Find the red blood cells and label each as P. falciparum-infected, uninfected, or of indeterminate infection status.
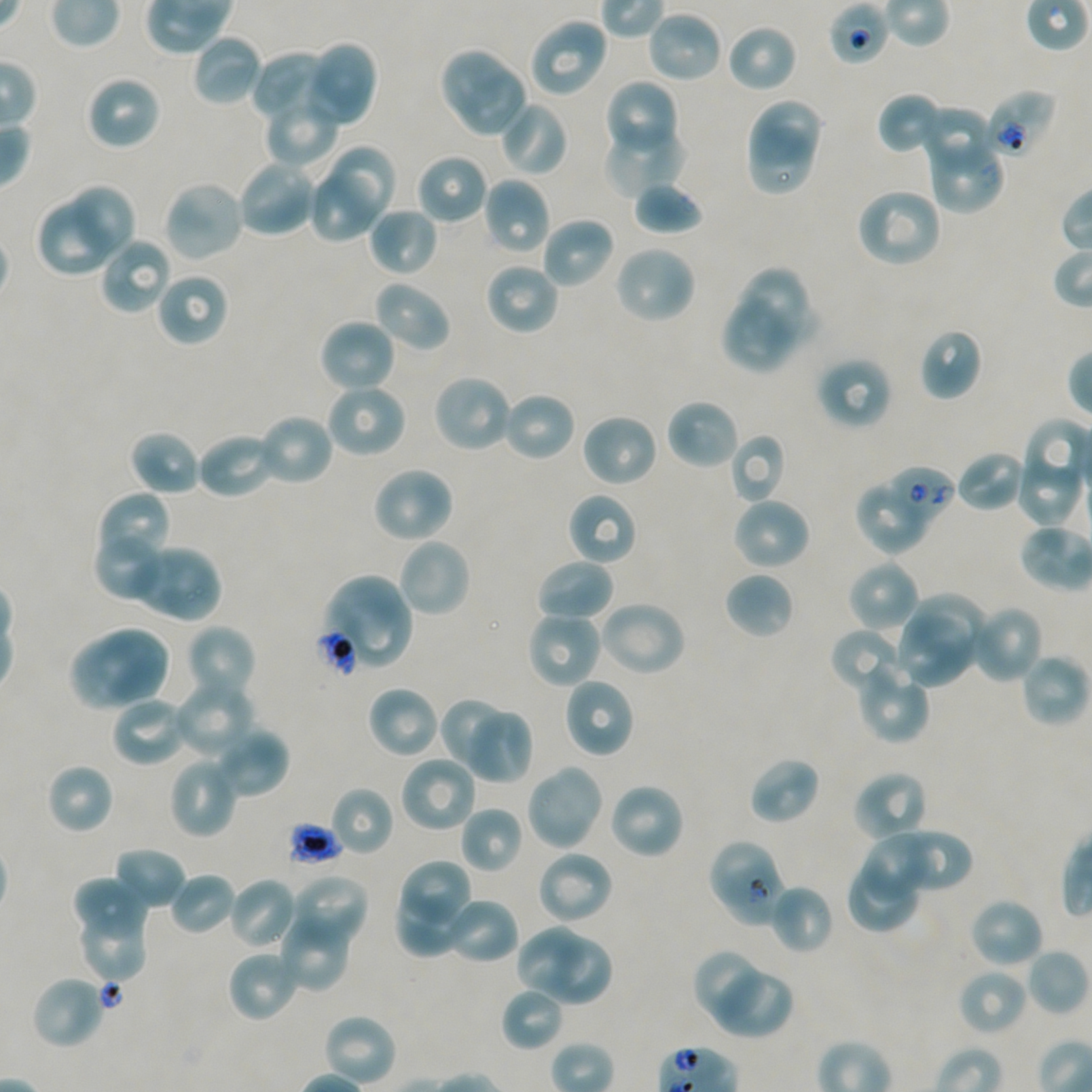

Approximate bounding boxes as {x1, y1, x2, y2} in pixels. Not every red blood cell is marked.
Red blood cells of indeterminate infection status: {829, 1, 891, 65}, {985, 89, 1057, 160}, {925, 134, 1004, 213}, {888, 465, 956, 522}, {315, 627, 359, 678}, {707, 837, 776, 911}, {726, 864, 785, 926}.
Uninfected red blood cells: {646, 10, 724, 84}, {528, 16, 608, 99}, {726, 23, 798, 94}, {192, 33, 263, 108}, {304, 41, 378, 128}, {438, 46, 509, 115}, {251, 50, 331, 123}, {458, 67, 526, 138}, {86, 75, 162, 151}, {603, 79, 680, 159}, {877, 92, 947, 155}, {263, 96, 339, 168}, {744, 96, 820, 165}, {498, 100, 569, 177}, {918, 103, 997, 173}, {602, 123, 686, 199}, {748, 130, 812, 193}, {329, 146, 396, 220}, {416, 153, 489, 225}, {236, 158, 319, 238}, {312, 175, 376, 241}, {481, 176, 551, 255}, {633, 179, 704, 236}, {162, 180, 246, 263}, {71, 185, 133, 256}, {855, 186, 943, 269}, {36, 200, 111, 278}, {368, 206, 439, 277}, {540, 216, 616, 290}, {98, 236, 173, 316}, {612, 244, 697, 325}, {484, 262, 560, 337}, {739, 266, 807, 338}, {155, 272, 230, 347}, {372, 280, 451, 353}, {721, 295, 794, 374}, {318, 317, 397, 394}, {919, 327, 983, 401}, {816, 356, 893, 431}, {432, 373, 515, 454}, {325, 382, 407, 459}, {501, 390, 577, 462}, {665, 397, 740, 471}, {255, 412, 335, 487}, {580, 412, 659, 488}, {128, 429, 202, 497}, {196, 431, 278, 500}, {729, 433, 788, 504}, {956, 450, 1027, 513}, {1015, 462, 1082, 526}, {370, 465, 455, 545}, {857, 486, 926, 553}, {98, 490, 166, 560}, {566, 491, 639, 566}, {731, 496, 811, 571}, {96, 535, 158, 597}, {397, 536, 472, 619}, {126, 543, 221, 623}, {535, 558, 615, 624}, {848, 559, 920, 633}, {723, 571, 795, 640}, {323, 573, 414, 672}, {913, 593, 985, 667}, {598, 600, 687, 678}, {969, 604, 1045, 684}, {526, 610, 602, 689}, {895, 612, 975, 688}, {184, 623, 257, 704}, {830, 627, 909, 695}, {95, 629, 168, 700}, {68, 638, 145, 712}, {1019, 653, 1089, 729}, {855, 659, 930, 744}, {562, 676, 636, 759}, {172, 677, 257, 759}, {367, 685, 441, 759}, {109, 694, 190, 768}, {438, 697, 509, 774}, {471, 711, 534, 784}, {213, 724, 290, 799}, {399, 754, 479, 834}, {748, 755, 820, 825}, {168, 757, 239, 839}, {45, 762, 115, 835}, {524, 763, 604, 852}, {852, 770, 929, 845}, {608, 782, 686, 861}, {329, 786, 395, 857}, {460, 805, 524, 874}, {903, 827, 972, 887}, {865, 833, 930, 903}, {112, 846, 187, 911}, {535, 849, 615, 926}, {404, 861, 468, 922}, {845, 865, 916, 934}, {169, 872, 237, 936}, {293, 874, 370, 946}, {228, 876, 300, 951}, {72, 877, 146, 938}, {768, 883, 835, 955}, {399, 886, 471, 956}, {441, 896, 520, 965}, {968, 896, 1044, 970}, {75, 898, 149, 983}, {276, 911, 352, 994}, {513, 924, 583, 993}, {549, 936, 612, 1005}, {227, 948, 302, 1023}, {1026, 948, 1089, 1017}, {694, 951, 759, 1019}, {714, 968, 793, 1037}, {957, 968, 1028, 1036}, {30, 974, 108, 1050}, {500, 986, 564, 1052}, {323, 1013, 397, 1087}.
No infected red blood cells observed.

Donor blood group A+/O+. Static in-vitro culture of P. falciparum strain NF54. Oil immersion, 100x objective (numerical aperture 1.45). Image is 1092×1092 pixels. Thin blood smear. One field from this slide. Giemsa-stained preparation.